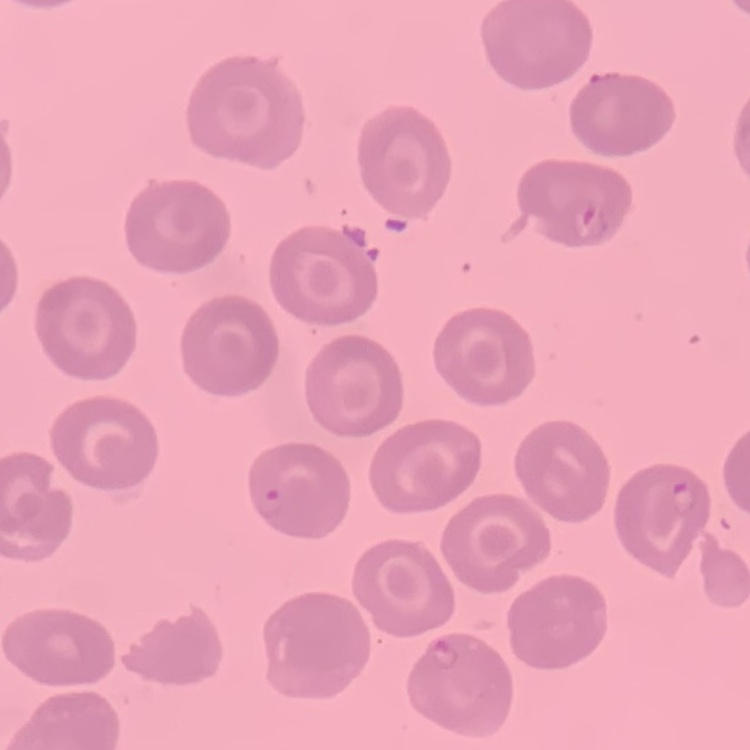

erythrocyte morphology = no rouleaux formation
preparation = thin peripheral smear
stain = Field's or Giemsa
image type = square crop of a larger photomicrograph